Assess this cell for malaria.
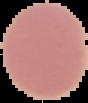

It is uninfected.

image_type: cell region segmented out of the field of view; surrounding area masked to black
preparation: thin blood film
image_size: 88×103 pixels